Classify this cell by malaria status.
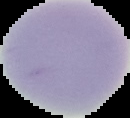

Uninfected.

{
  "image_type": "segmented cell region on a black background",
  "preparation": "thin blood smear",
  "image_size": "130×118 pixels"
}